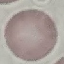
Summary:
  - Result: no malaria parasites seen
  - Capture: smartphone through the microscope eyepiece
  - Preparation: thin blood film
  - Image type: cell patch, automatically extracted from a larger field of view and resized to 64 × 64 pixels
  - Stain: Giemsa